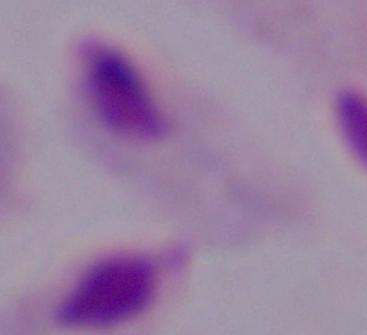
Summary:
  - Identification: trichomonad
  - Modality: photomicrograph
  - Magnification: 1000x